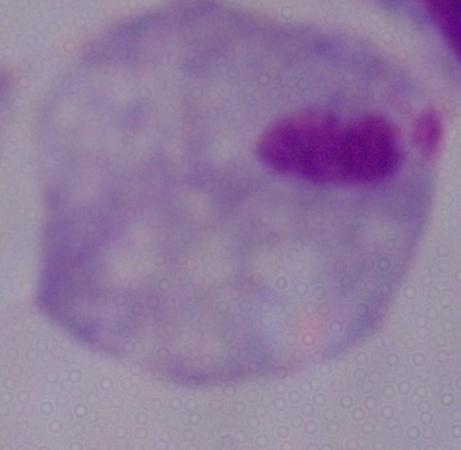
A trichomonad is shown. Micrograph. Captured at 1000x magnification.